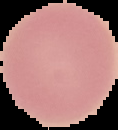
preparation = thin blood smear
image type = cell region segmented out of the field of view; surrounding area masked to black
result = no Plasmodium parasites detected
image size = 118×130 pixels